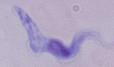
magnification = 1000x
modality = micrograph
identification = trypanosome